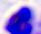

modality = photomicrograph
magnification = 400x
identification = leukocyte